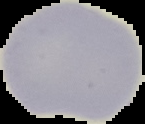
{
  "preparation": "thin blood film",
  "image_size": "145×124 pixels",
  "malaria_status": "uninfected",
  "image_type": "segmented cell region with the area outside set to black"
}